Evaluate for malaria.
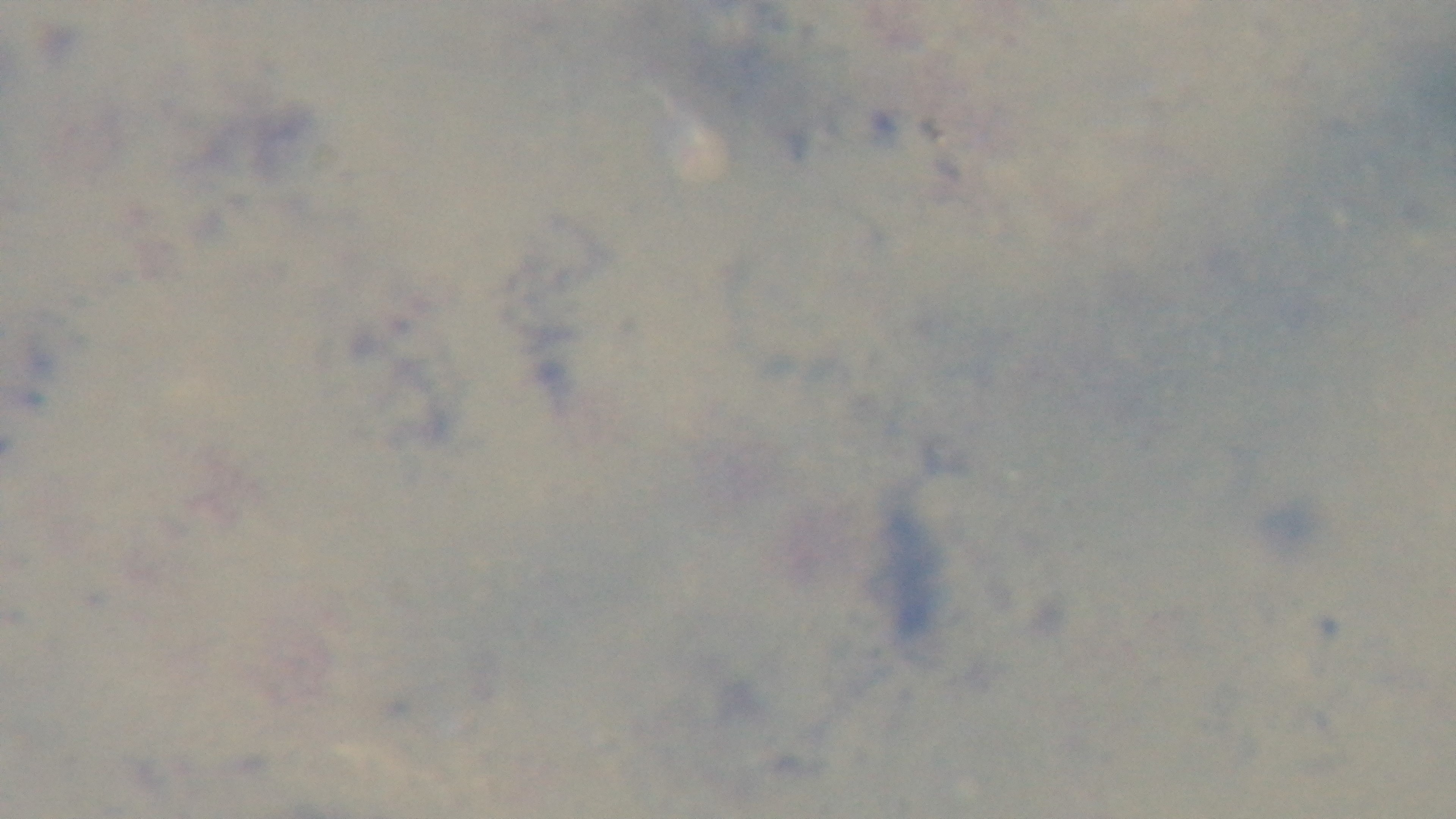
Negative.

Mounted 4K digital camera. Giemsa stain. Light microscopy. One field from the slide. Oil-immersion objective, 100x. Preparation: thick.